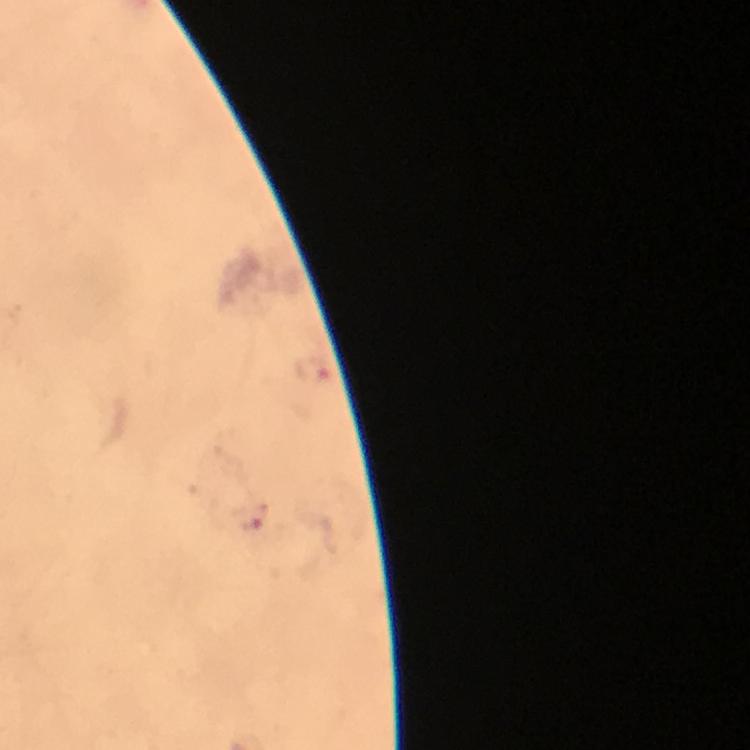

capture = smartphone camera through the microscope
immersion oil = applied
preparation = thick smear
cropped from = one field of view
malaria parasite locations = approximate centers as [x, y] in pixels: [314, 370], [251, 520]
magnification = 100x
context = from a malaria diagnostic workup
image size = 750×750 pixels
stain = Giemsa